Find the red blood cells and label each as P. falciparum-infected, uninfected, or of indeterminate infection status.
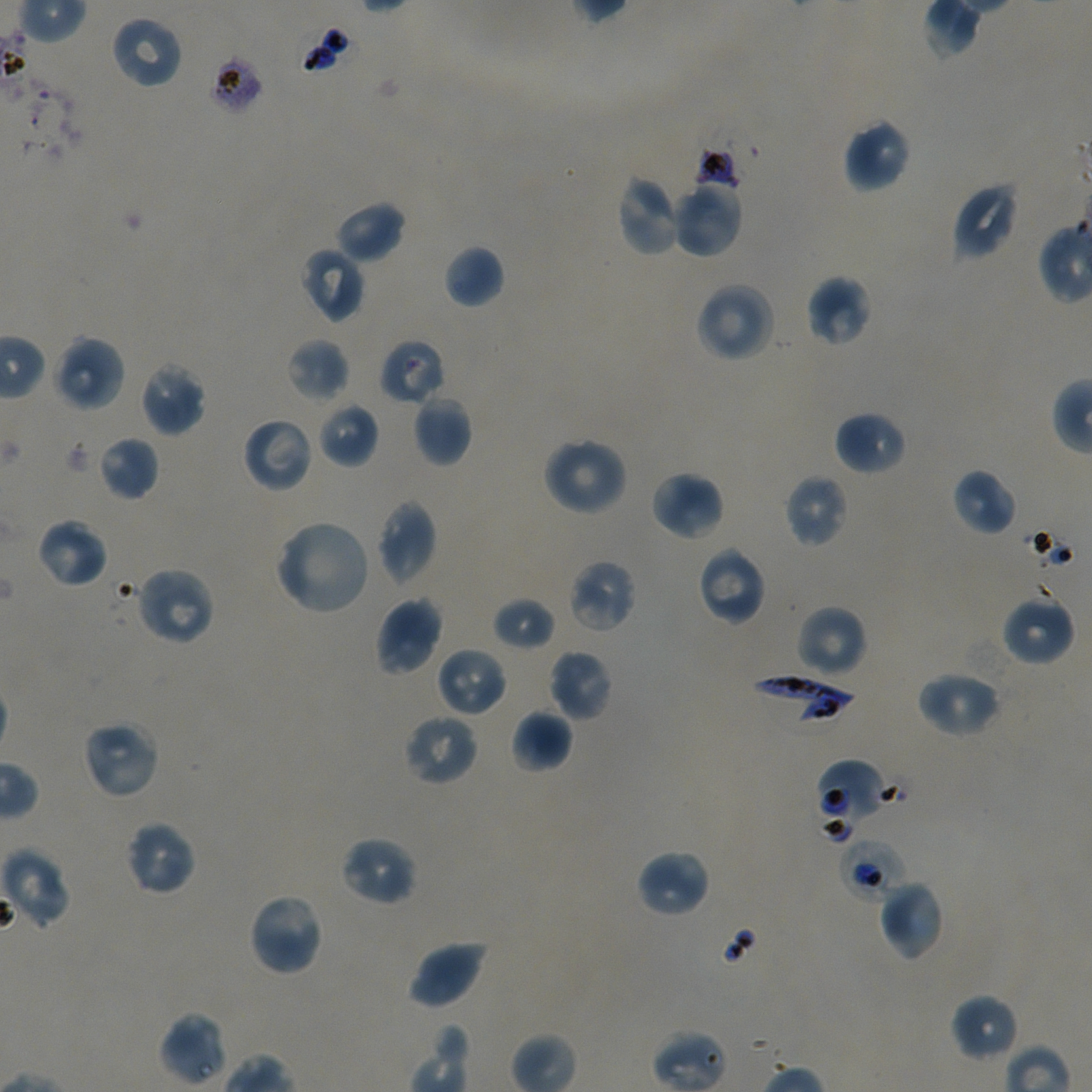

Approximate bounding rectangles given as corner coordinates in pixels from the top-left. Not every red blood cell is marked. A life-cycle stage — or a range of stages, where the recorded stages span more than one — follows each staged infected red blood cell.
Infected red blood cells: (x1=747, y1=673, x2=856, y2=724); (x1=838, y1=837, x2=908, y2=902) early trophozoite.
Red blood cells of indeterminate infection status: (x1=209, y1=53, x2=265, y2=115), (x1=379, y1=338, x2=445, y2=406), (x1=815, y1=759, x2=888, y2=835), (x1=652, y1=1030, x2=728, y2=1092).
Uninfected red blood cells: (x1=109, y1=15, x2=184, y2=90), (x1=842, y1=117, x2=912, y2=194), (x1=615, y1=173, x2=683, y2=257), (x1=670, y1=179, x2=743, y2=259), (x1=951, y1=181, x2=1019, y2=261), (x1=333, y1=200, x2=406, y2=265), (x1=443, y1=244, x2=505, y2=308), (x1=298, y1=247, x2=366, y2=323), (x1=805, y1=275, x2=873, y2=347), (x1=694, y1=282, x2=775, y2=363), (x1=53, y1=333, x2=127, y2=412), (x1=286, y1=338, x2=350, y2=401), (x1=139, y1=361, x2=206, y2=437), (x1=412, y1=394, x2=473, y2=467), (x1=316, y1=401, x2=379, y2=469), (x1=833, y1=410, x2=907, y2=475), (x1=241, y1=416, x2=314, y2=493), (x1=97, y1=435, x2=160, y2=501), (x1=542, y1=436, x2=629, y2=516), (x1=951, y1=468, x2=1017, y2=536), (x1=649, y1=470, x2=725, y2=543), (x1=784, y1=474, x2=849, y2=547), (x1=376, y1=498, x2=438, y2=588), (x1=36, y1=517, x2=109, y2=589), (x1=274, y1=519, x2=372, y2=616), (x1=696, y1=545, x2=767, y2=626), (x1=567, y1=559, x2=637, y2=634), (x1=135, y1=566, x2=215, y2=647), (x1=1000, y1=593, x2=1076, y2=666), (x1=374, y1=596, x2=444, y2=676), (x1=492, y1=596, x2=555, y2=651), (x1=795, y1=604, x2=868, y2=678), (x1=435, y1=646, x2=509, y2=718), (x1=547, y1=649, x2=615, y2=721), (x1=915, y1=670, x2=1002, y2=738), (x1=510, y1=709, x2=572, y2=773), (x1=402, y1=712, x2=480, y2=787), (x1=81, y1=719, x2=160, y2=799), (x1=124, y1=820, x2=198, y2=896), (x1=338, y1=835, x2=418, y2=907), (x1=1, y1=848, x2=70, y2=929), (x1=634, y1=850, x2=711, y2=918), (x1=877, y1=879, x2=945, y2=962), (x1=248, y1=892, x2=325, y2=977), (x1=407, y1=938, x2=489, y2=1010), (x1=949, y1=993, x2=1019, y2=1063), (x1=158, y1=1012, x2=228, y2=1087).

{
  "stain": "Giemsa",
  "objective": "100x, oil immersion, numerical aperture 1.45",
  "image_size": "1092×1092 pixels",
  "preparation": "thin blood smear",
  "culture": "in-vitro P. falciparum strain NF54, static",
  "field_of_view": "one from this slide",
  "donor_blood_group": "A+/O+"
}